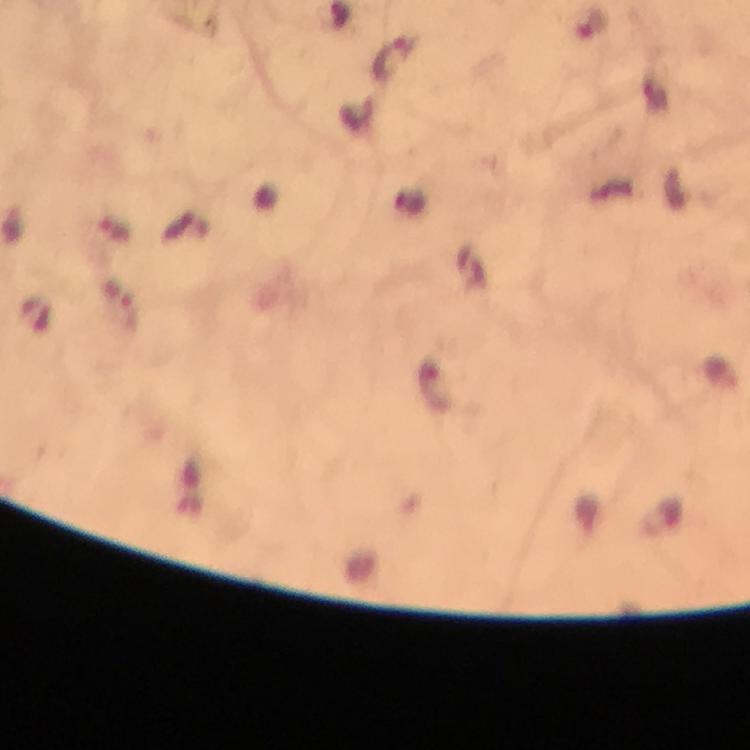

Approximate centers as [x, y] in pixels.
Summary:
  - Malaria parasite locations: [392, 60], [118, 229], [122, 305]
  - Context: from a diagnostic examination for malaria
  - Stain: Giemsa
  - Cropped from: a single field of view
  - Image size: 750×750 pixels
  - Preparation: thick blood film
  - Capture: smartphone mounted on the microscope
  - Magnification: 100x
  - Immersion oil: used